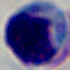 Photomicrograph. 1000x magnification. A white blood cell is seen.